Assess this cell for malaria.
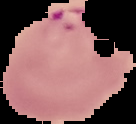
Parasitized.

{
  "image_size": "136×124 pixels",
  "image_type": "segmented cell region on a black background",
  "preparation": "thin blood film"
}